Assess this cell for malaria.
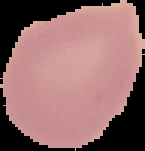
Uninfected.

From a thin blood film. The area outside the segmented cell region is set to black. Image is 145×151 pixels.